Classify this cell by malaria status.
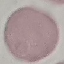
It is uninfected.

Summary:
  - Capture: smartphone through the microscope eyepiece
  - Image type: automatically extracted cell patch, resized to 64 × 64 pixels
  - Stain: Giemsa
  - Preparation: thin blood film